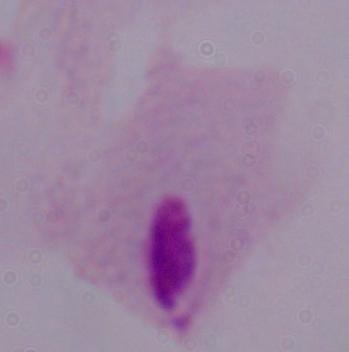

Micrograph. A trichomonad is shown. 1000x magnification.